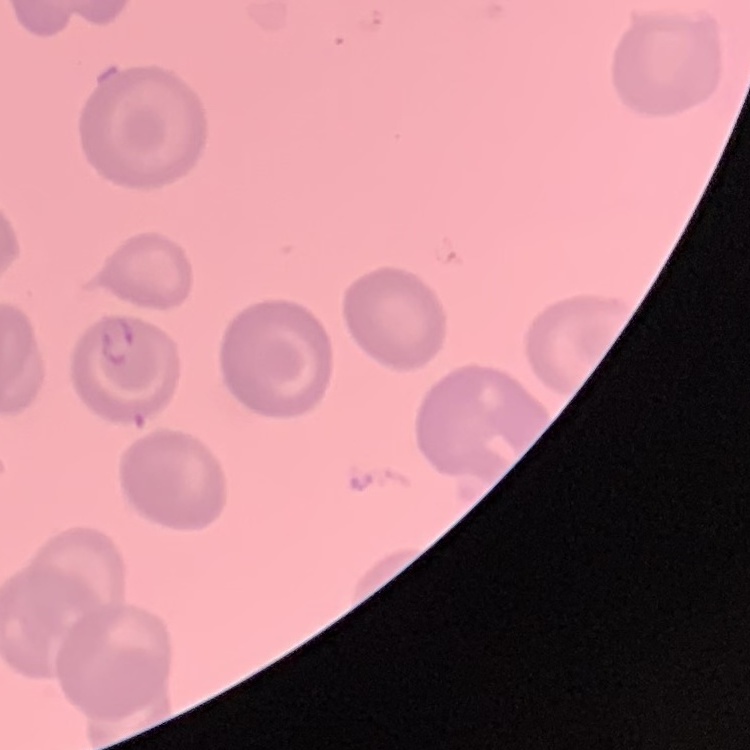
{
  "red_blood_cell_morphology": "no rouleaux formation",
  "preparation": "thin blood smear",
  "image_type": "one tile cut from a larger photomicrograph",
  "stain": "Field's or Giemsa"
}